Report the malaria status of this cell.
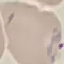
It is parasitized.

capture: smartphone through the microscope eyepiece
image_type: cell patch, automatically extracted from a larger field of view and resized to 64 × 64 pixels
stain: Giemsa
preparation: thin blood smear